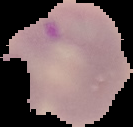

Malaria status: parasitized. Image is 133×127 pixels. From a thin blood smear. The area outside the segmented cell region is set to black.